Identify the parasite.
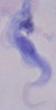
A trypanosome.

modality = micrograph
magnification = 1000x